Classify this cell by malaria status.
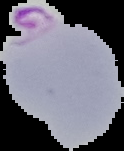
Parasitized.

Cell region segmented out of the field of view; the surrounding area is masked to black. From a thin blood film. Image is 124×151 pixels.